Name the parasite shown.
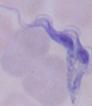

A trypanosome.

magnification = 1000x
modality = micrograph